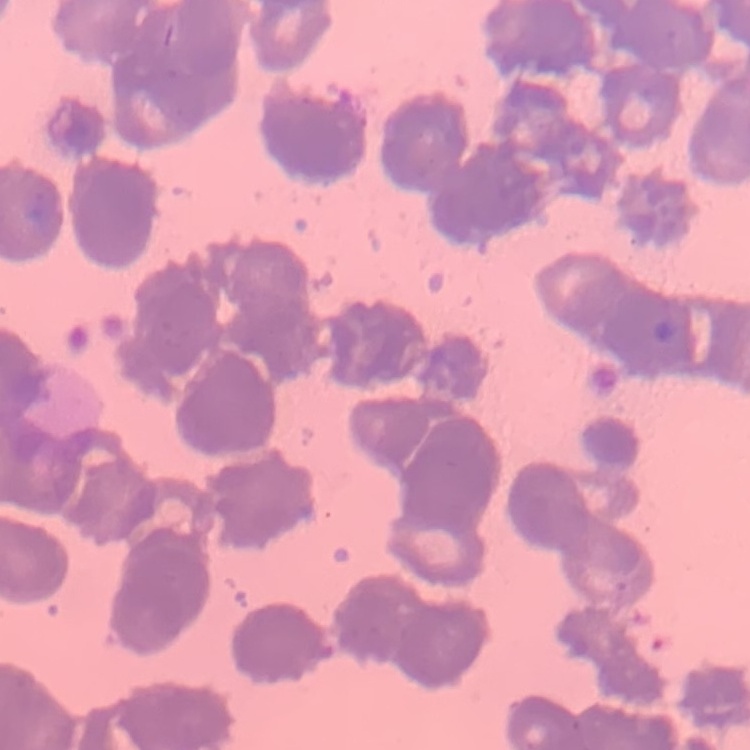
The red blood cells show rouleaux formation. Square crop of a larger photomicrograph. Stained with either Field's or Giemsa. Thin peripheral smear.